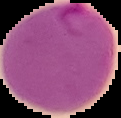
Image is 121×118 pixels. From a thin blood film. Cell region segmented out of the field of view; the surrounding area is masked to black. Result: Plasmodium parasites identified.